Assess the morphology of the red blood cells.
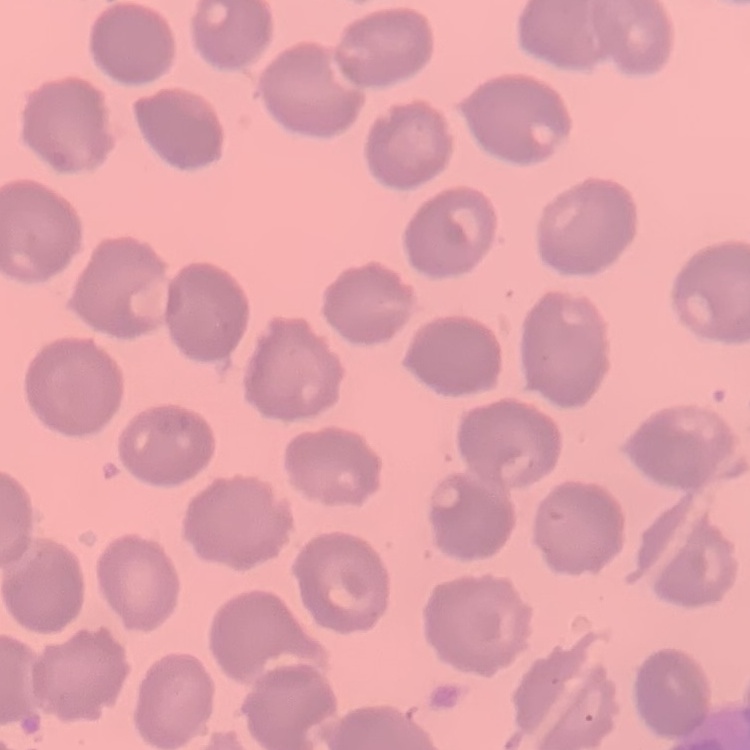
No rouleaux formation.

Thin blood film. Square crop of a larger photomicrograph. Field's or Giemsa stain.